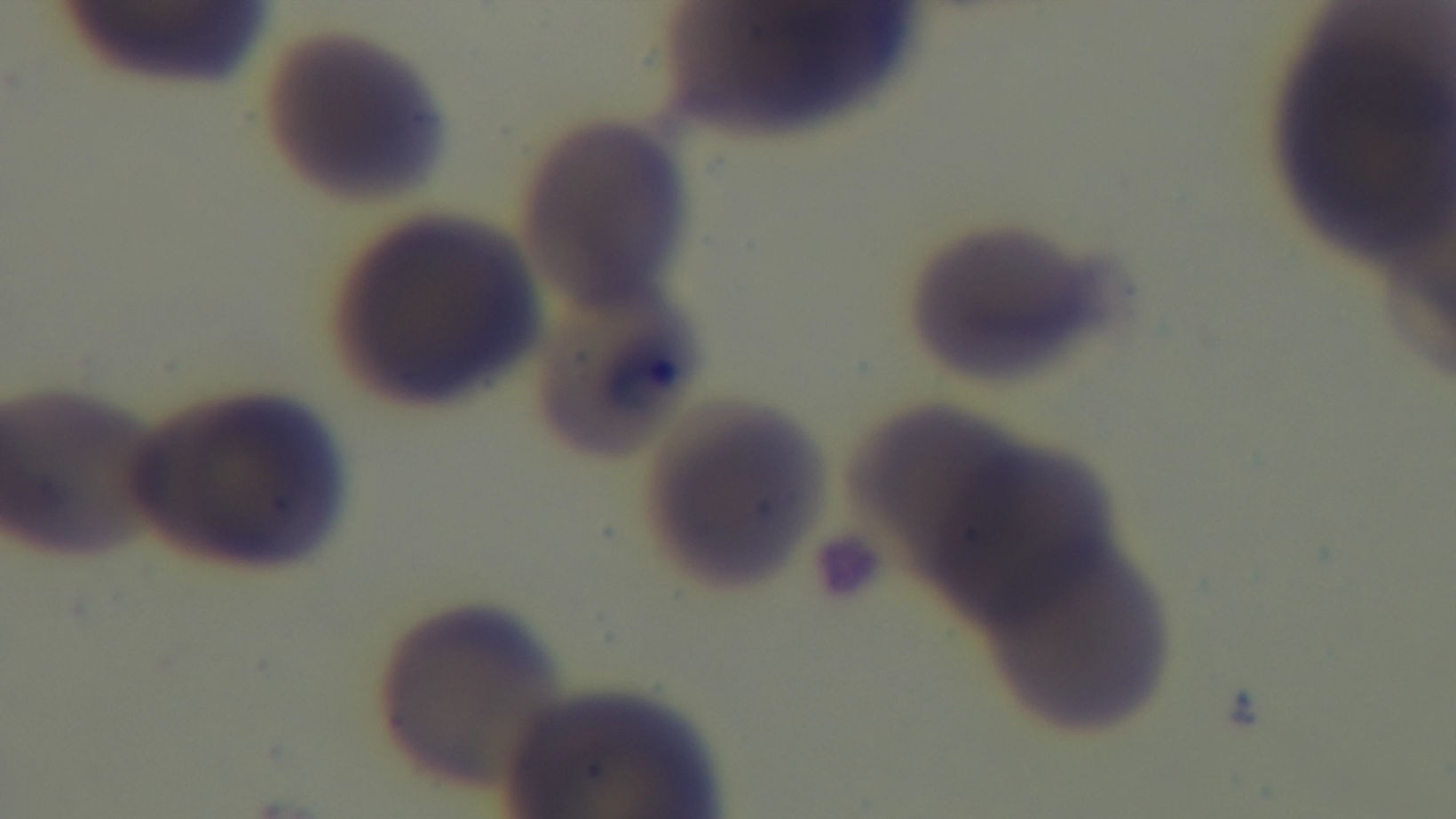

capture: mounted 4K digital camera
stain: Giemsa
modality: light microscopy
field_of_view: one from the slide
objective: 100x oil immersion
preparation: thin smear
malaria_status: infected